Draw a bounding box around every Plasmodium parasite.
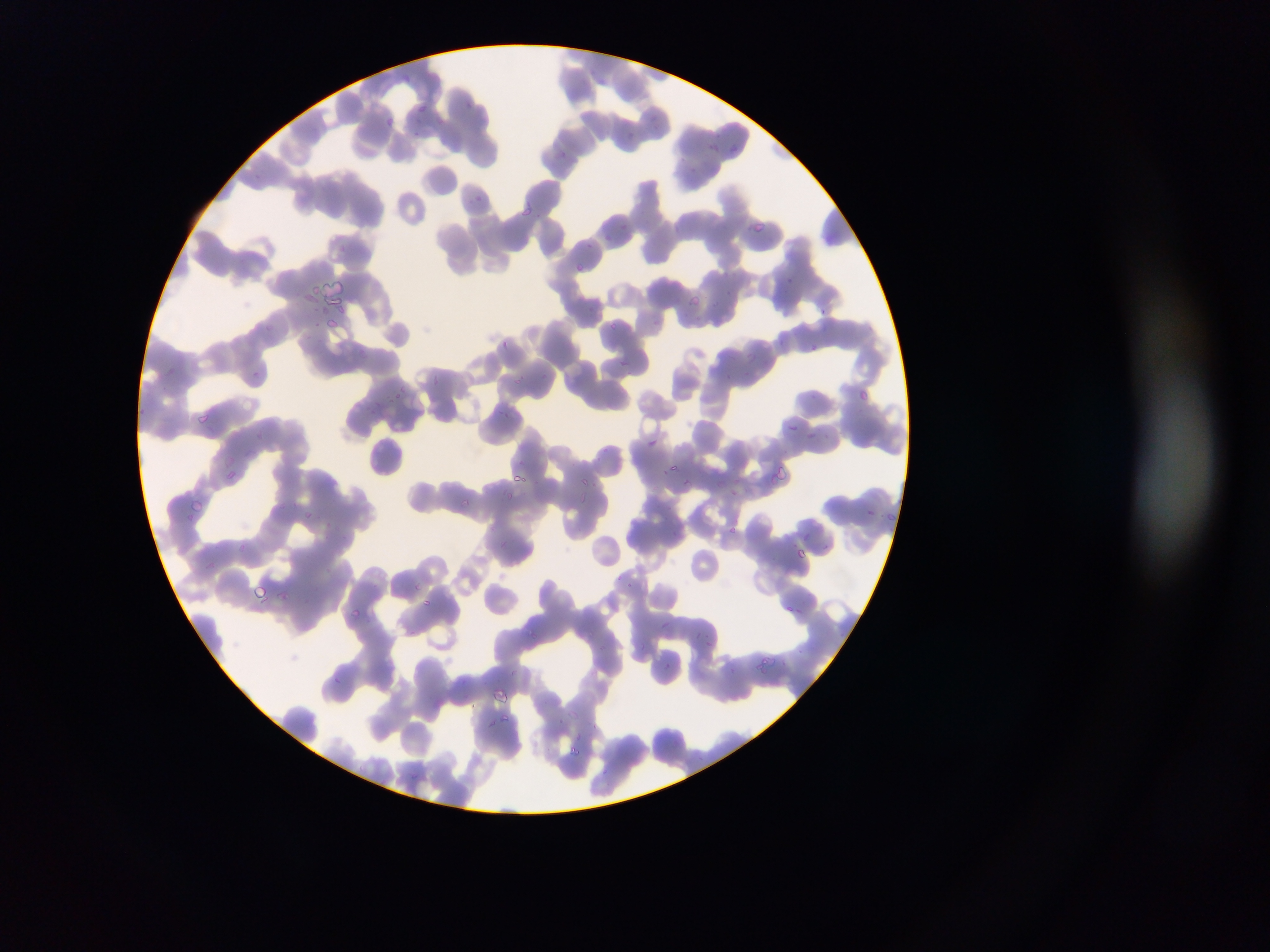
Approximate bounding boxes as left top right bottom in pixels.
Plasmodium parasites: 417 98 437 116; 381 114 397 131; 725 138 744 159; 706 143 727 159; 554 150 575 162; 471 192 488 207; 518 202 533 220; 748 218 769 237; 621 220 639 236; 585 236 596 252; 568 260 583 274; 312 284 319 296; 690 291 711 309; 819 305 847 327; 650 315 668 333; 326 318 339 330; 499 339 511 351; 613 352 641 372; 253 368 267 385; 434 377 449 393; 856 383 872 406; 387 384 419 404; 195 413 210 425; 786 423 802 434; 807 429 823 441; 647 433 660 446; 664 461 684 478; 776 464 798 485; 227 469 237 481; 681 473 703 490; 509 475 529 488; 728 483 742 500; 458 496 472 510; 193 500 208 520; 860 503 882 524; 884 507 904 529; 724 523 744 541; 791 545 818 564; 614 568 646 594; 248 582 275 606; 424 596 434 609; 349 602 366 619; 778 603 808 618; 659 615 674 627; 525 625 536 642; 754 658 772 676; 663 660 670 669; 492 685 513 702; 566 710 581 722; 497 713 518 727; 568 741 581 759.

Summary:
  - Image size: 1270×952 pixels
  - Capture: mobile-phone photograph through a microscope
  - Preparation: thin blood smear
  - Country: Ghana
  - Field of view: single